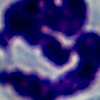
Summary:
  - Magnification: 1000x
  - Identification: white blood cell
  - Modality: micrograph